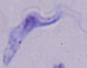

modality = micrograph
magnification = 1000x
identification = trypanosome